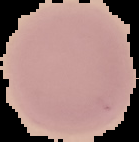

Cell region segmented out of the field of view; the surrounding area is masked to black. From a thin blood film. Image is 139×142 pixels. Malaria status: uninfected.